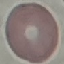 Malaria status: uninfected. Photographed with a smartphone camera at the microscope eyepiece. Giemsa-stained preparation. Automatically extracted cell patch, resized to 64 × 64 pixels. Thin blood film.